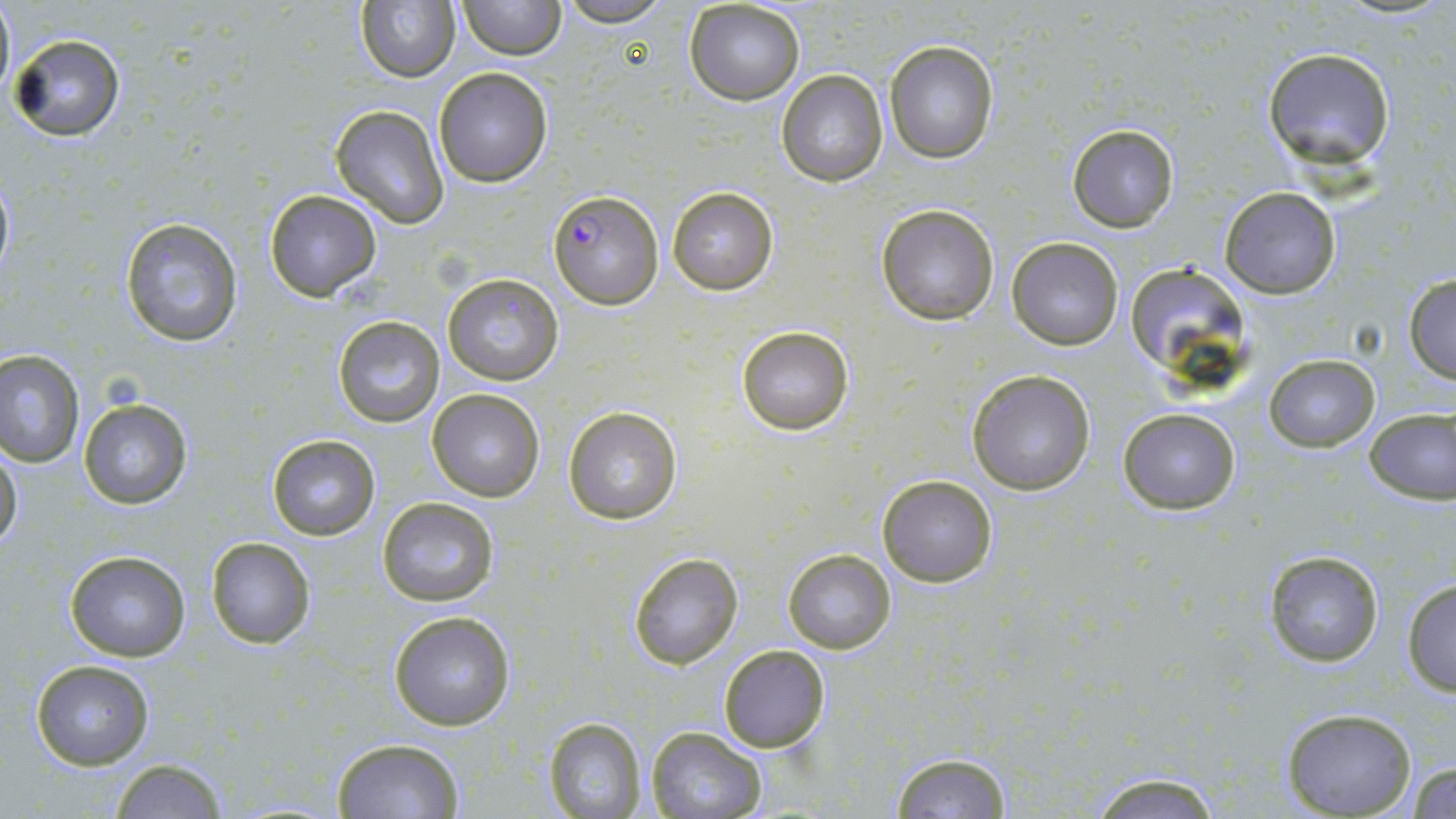
{
  "plasmodium_falciparum_infected_red_blood_cell_locations": "approximate bounding boxes as (x1,y1)-(x2,y2) corner pairs in pixels: (549,190)-(662,308)",
  "slide_level_diagnosis": "Plasmodium falciparum",
  "uninfected_red_blood_cell_locations": "approximate bounding boxes as (x1,y1)-(x2,y2) corner pairs in pixels: (0,0)-(16,101), (356,0)-(462,83), (457,0)-(565,59), (553,0)-(673,27), (684,2)-(806,105), (10,33)-(127,141), (883,40)-(998,164), (1263,48)-(1397,170), (433,66)-(555,186), (777,69)-(888,187), (331,104)-(448,225), (1067,123)-(1180,232), (0,174)-(14,282), (666,185)-(779,296), (1219,187)-(1341,297), (263,189)-(383,302), (877,203)-(1000,325), (119,217)-(244,347), (1007,237)-(1123,350), (1122,265)-(1249,381), (1403,272)-(1456,383), (442,273)-(564,387), (333,314)-(447,427), (735,324)-(855,437), (0,350)-(82,466), (1264,354)-(1378,451), (967,369)-(1096,495), (426,389)-(545,503), (77,397)-(194,512), (1363,405)-(1455,506), (563,406)-(682,525), (1117,406)-(1241,513), (266,432)-(381,542), (0,448)-(23,553), (877,474)-(998,587), (377,497)-(498,606), (205,536)-(317,650), (783,548)-(895,655), (1261,548)-(1384,668), (63,549)-(191,661), (627,552)-(744,671), (1403,577)-(1456,697), (388,609)-(517,731), (717,644)-(832,752), (29,659)-(155,770), (1280,709)-(1418,819), (544,717)-(647,818), (645,727)-(767,818), (331,738)-(465,819), (890,752)-(1014,818), (108,759)-(230,817), (1407,761)-(1456,818), (1082,770)-(1226,817)",
  "stain": "May-Grünwald-Giemsa",
  "modality": "optical microscopy",
  "magnification": "1000x",
  "field_of_view": "one of a larger specimen",
  "preparation": "thin blood film",
  "image_size": "1456×819 pixels"
}